Assess this cell for malaria.
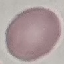

Uninfected.

stain = Giemsa
capture = smartphone through the microscope eyepiece
preparation = thin smear
image type = automatically extracted cell patch, resized to 64 × 64 pixels